Identify the blood parasite species.
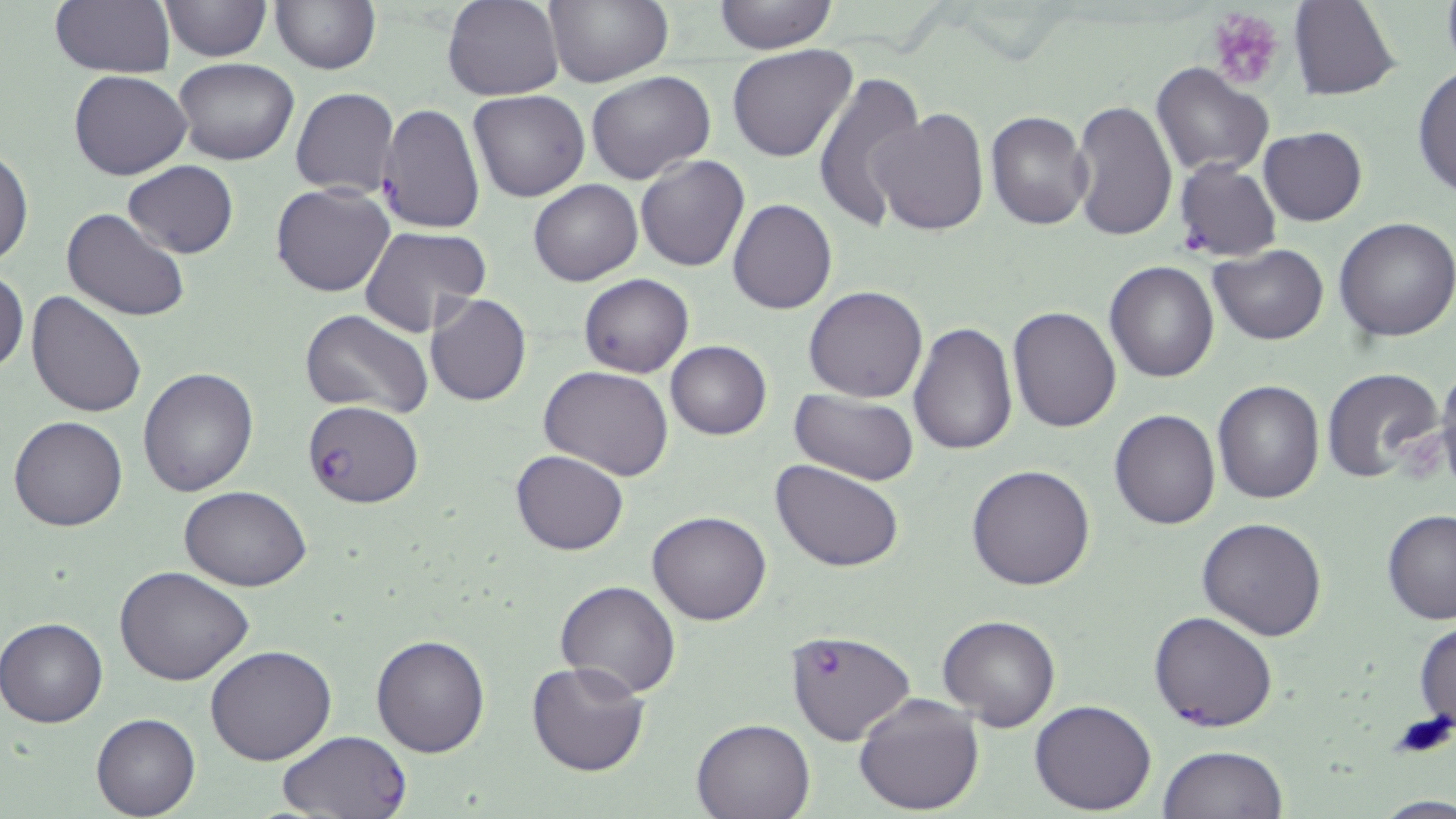

Plasmodium falciparum.

preparation: thin blood film
modality: optical microscopy
magnification: 1000x
platelet_locations: 'approximate bounding boxes as (x1, y1, x2, y2) in pixels: (1206, 9, 1287, 91)'
image_size: 1456×819 pixels
plasmodium_falciparum_infected_red_blood_cell_locations: 'approximate bounding boxes as (x1, y1, x2, y2) in pixels: (301, 399, 424, 507), (1148, 610, 1278, 732), (785, 628, 915, 746), (277, 730, 413, 817)'
uninfected_red_blood_cell_locations: 'approximate bounding boxes as (x1, y1, x2, y2) in pixels: (158, 0, 270, 61), (442, 0, 565, 101), (544, 0, 673, 87), (713, 0, 836, 53), (49, 1, 174, 76), (270, 1, 380, 74), (1289, 1, 1400, 100), (727, 45, 859, 164), (174, 58, 301, 166), (1151, 62, 1274, 178), (1414, 64, 1455, 200), (69, 69, 192, 181), (585, 70, 716, 185), (812, 70, 925, 231), (290, 88, 399, 198), (468, 91, 591, 203), (1070, 100, 1178, 242), (376, 103, 486, 232), (870, 108, 989, 236), (984, 109, 1092, 231), (1258, 128, 1367, 226), (0, 144, 33, 268), (636, 155, 749, 272), (1172, 156, 1281, 263), (123, 160, 238, 258), (529, 178, 642, 286), (270, 184, 395, 298), (728, 199, 837, 315), (60, 207, 189, 321), (1333, 216, 1456, 341), (360, 225, 491, 336), (1209, 245, 1327, 345), (1104, 261, 1220, 383), (0, 268, 27, 376), (578, 273, 694, 378), (804, 285, 929, 402), (25, 291, 148, 419), (425, 293, 531, 406), (1008, 305, 1121, 431), (302, 309, 434, 419), (908, 322, 1018, 457), (664, 340, 771, 440), (1433, 363, 1456, 487), (540, 365, 676, 481), (1321, 365, 1445, 484), (138, 368, 260, 499), (1213, 379, 1324, 503), (790, 391, 920, 485), (1109, 408, 1220, 529), (9, 416, 127, 532), (510, 450, 629, 556), (771, 458, 905, 572), (966, 464, 1096, 591), (179, 486, 311, 591), (1381, 509, 1456, 623), (647, 511, 772, 625), (1197, 517, 1327, 640), (114, 564, 255, 686), (554, 580, 682, 699), (936, 614, 1060, 733), (0, 616, 108, 728), (1414, 619, 1456, 732), (371, 632, 490, 757), (206, 644, 337, 766), (525, 661, 650, 777), (853, 692, 985, 814), (1029, 699, 1156, 815), (92, 714, 199, 818), (692, 716, 816, 819), (1158, 745, 1288, 819), (1374, 796, 1456, 818)'
field_of_view: single
stain: May-Grünwald-Giemsa